Report the malaria status of this cell.
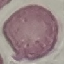

Uninfected.

Summary:
  - Capture: smartphone through the microscope eyepiece
  - Preparation: thin blood film
  - Stain: Giemsa
  - Image type: cell patch, automatically extracted from a larger field of view and resized to 64 × 64 pixels